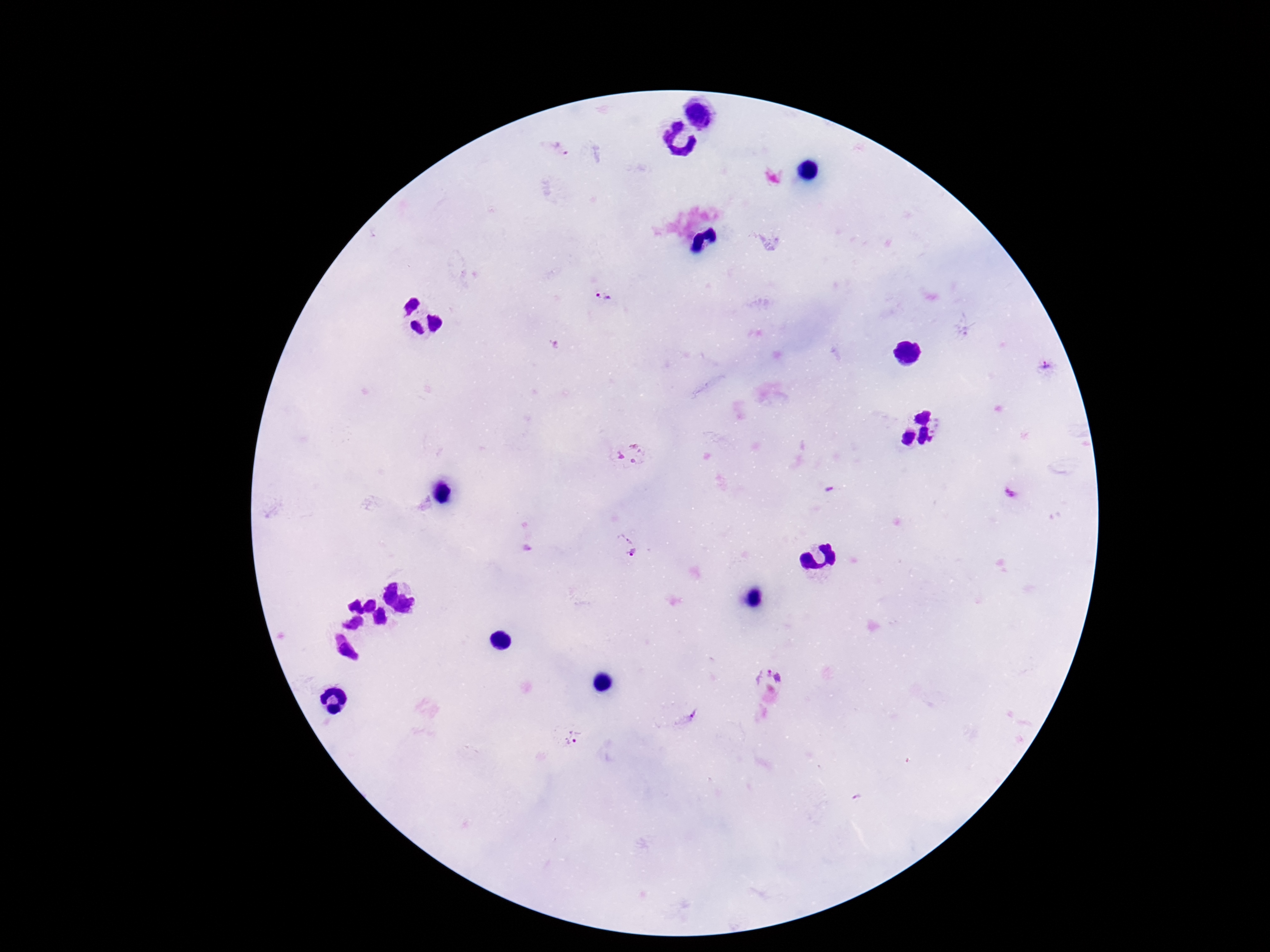

Approximate centers as [x, y] in pixels. Plasmodium parasite locations: [561, 149], [604, 298], [1046, 370], [632, 452], [830, 492], [1010, 494], [630, 549], [768, 675], [692, 719], [573, 739], [860, 798]. Thick peripheral-blood smear. Single field of view. Patient malaria status: positive. Giemsa-stained preparation. 100x magnification. Smartphone photograph taken through the microscope eyepiece. Image is 1270×952 pixels.